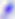
Captured at 400x magnification. Photomicrograph. Toxoplasma gondii is seen.